State which parasite is depicted.
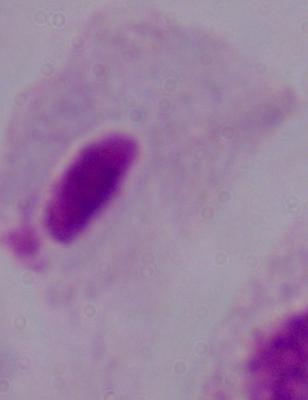
This is a trichomonad.

{
  "modality": "photomicrograph",
  "magnification": "1000x"
}